Assess this cell for malaria.
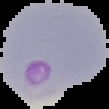

It is parasitized.

Image is 109×109 pixels. Segmented cell region on a black background. From a thin blood film.